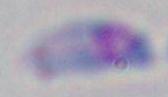
Toxoplasma gondii is shown. 1000x magnification. Photomicrograph.